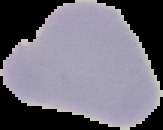

Summary:
  - Preparation: thin blood film
  - Image type: segmented cell region with the area outside set to black
  - Image size: 163×130 pixels
  - Malaria status: uninfected